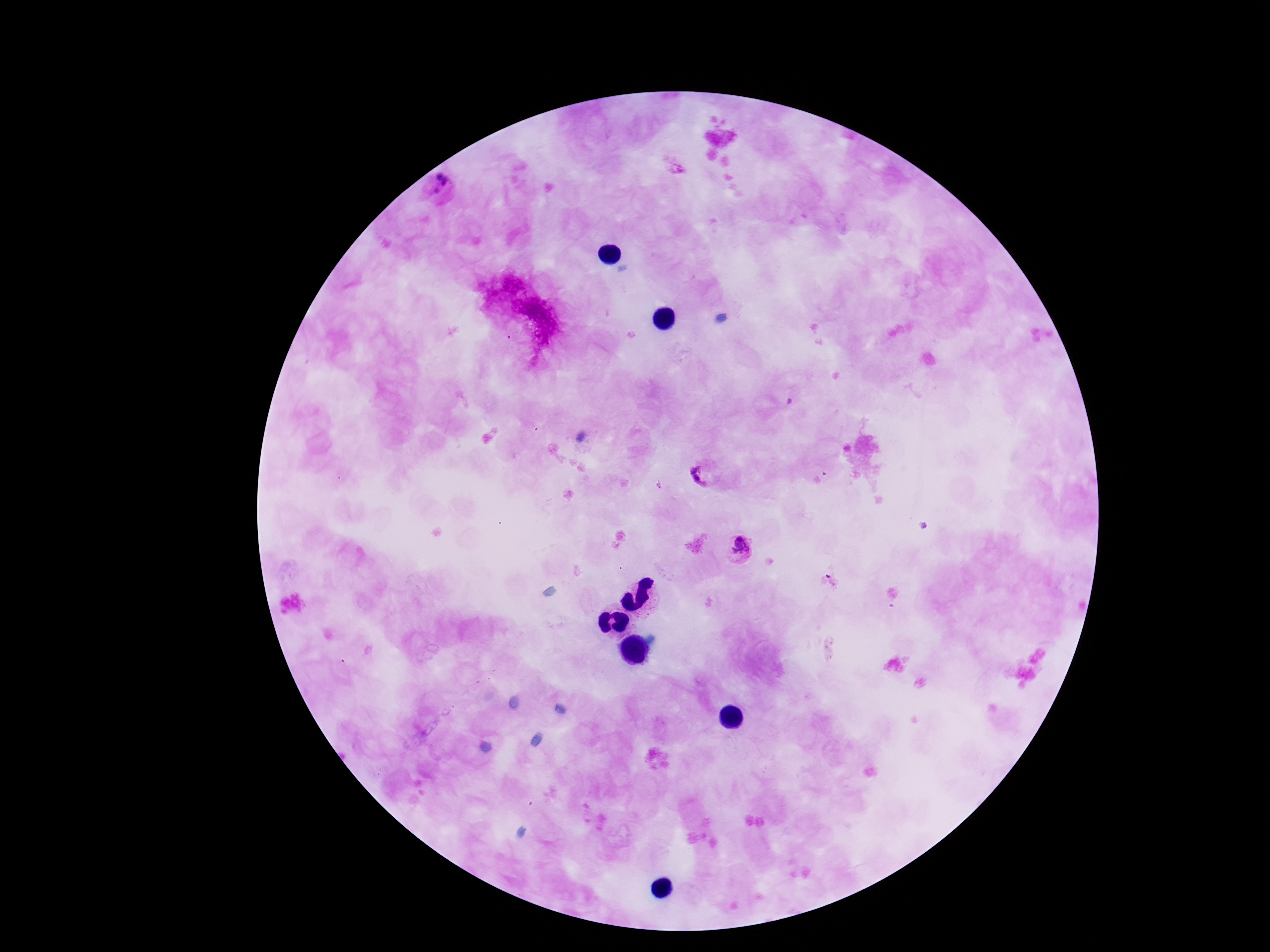
capture: smartphone camera through the microscope eyepiece
plasmodium_parasite_locations: 'approximate centers as [x, y] in pixels: [442, 190], [703, 476], [738, 548]'
image_size: 1270×952 pixels
patient_malaria_status: infected
preparation: thick blood smear
magnification: 100x
field_of_view: single
stain: Giemsa